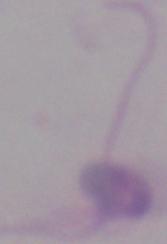 Micrograph. A Leishmania parasite is seen. Captured at 1000x magnification.